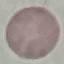
Summary:
  - Malaria status: uninfected
  - Stain: Giemsa
  - Image type: cell patch, automatically extracted from a larger field of view and resized to 64 × 64 pixels
  - Preparation: thin blood smear
  - Capture: smartphone through the microscope eyepiece